Name the parasite shown.
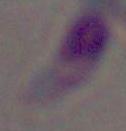

Toxoplasma gondii.

Captured at 1000x magnification. Micrograph.